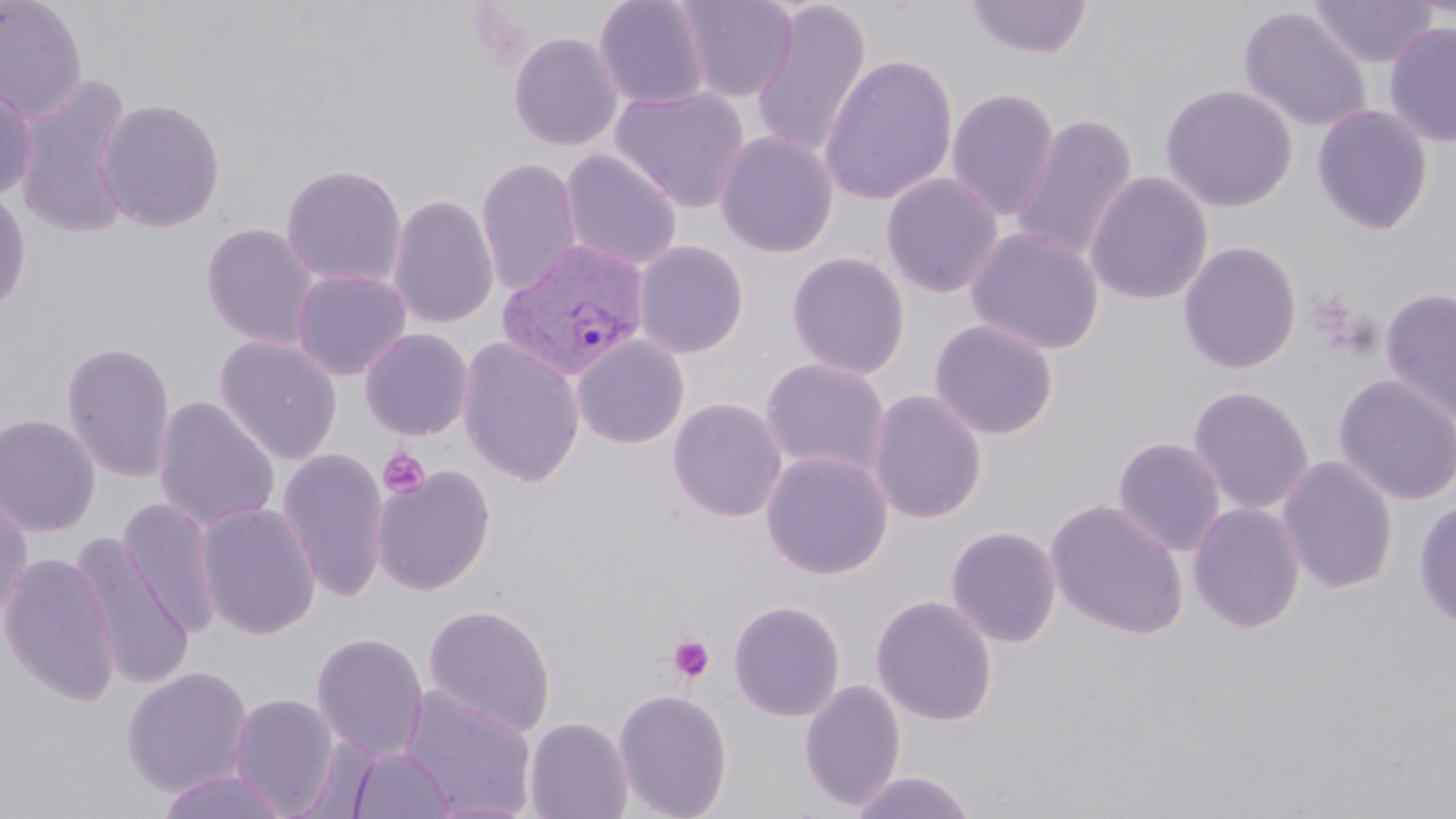
Summary:
  - Coordinate format: approximate bounding boxes as (x1, y1, x2, y2) in pixels
  - Uninfected red blood cell locations: (0, 0, 89, 122), (593, 0, 713, 110), (674, 0, 798, 103), (964, 0, 1094, 60), (1308, 0, 1437, 68), (750, 2, 872, 160), (1237, 6, 1372, 133), (1383, 21, 1456, 148), (508, 31, 624, 152), (818, 54, 959, 206), (11, 74, 137, 239), (0, 80, 38, 205), (1160, 83, 1297, 212), (610, 86, 750, 214), (946, 87, 1060, 222), (96, 98, 226, 233), (1312, 104, 1434, 236), (1009, 113, 1138, 263), (715, 130, 838, 258), (559, 149, 683, 271), (475, 157, 582, 296), (280, 164, 407, 288), (1083, 171, 1213, 305), (881, 172, 1004, 298), (0, 185, 32, 317), (388, 194, 499, 330), (201, 222, 321, 349), (965, 226, 1105, 355), (633, 240, 750, 360), (1177, 241, 1302, 374), (786, 251, 910, 380), (291, 269, 412, 381), (1380, 287, 1456, 425), (929, 318, 1059, 440), (359, 327, 474, 441), (214, 335, 343, 465), (571, 335, 690, 449), (457, 336, 586, 487), (61, 340, 176, 483), (760, 358, 891, 477), (1333, 373, 1456, 507), (1188, 385, 1315, 515), (866, 389, 987, 525), (153, 395, 280, 533), (667, 397, 788, 523), (0, 413, 101, 537), (1112, 437, 1226, 556), (277, 446, 389, 603), (761, 450, 893, 580), (1276, 454, 1399, 594), (371, 464, 496, 597), (0, 488, 34, 625), (118, 496, 224, 638), (1414, 498, 1456, 632), (1045, 499, 1188, 639), (1187, 501, 1306, 633), (196, 502, 321, 639), (945, 525, 1062, 647), (71, 534, 195, 690), (0, 551, 120, 706), (871, 594, 998, 727), (728, 599, 846, 722), (422, 603, 557, 737), (311, 632, 429, 761), (120, 666, 254, 797), (799, 679, 906, 812), (399, 685, 538, 818), (612, 688, 733, 819), (228, 694, 343, 816), (523, 716, 633, 819), (346, 745, 456, 818), (155, 769, 292, 819), (848, 770, 979, 819)
  - Plasmodium vivax-infected red blood cell locations: (497, 237, 651, 382)
  - Platelet locations: (378, 448, 431, 499), (667, 634, 716, 683)
  - Slide-level diagnosis: Plasmodium vivax
  - Magnification: 1000x
  - Preparation: thin blood film
  - Field of view: one of a larger specimen
  - Modality: light microscopy
  - Stain: May-Grünwald-Giemsa
  - Image size: 1456×819 pixels